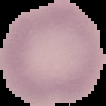

malaria status = uninfected
image size = 106×106 pixels
image type = segmented cell region with the area outside set to black
preparation = thin blood smear